Report the malaria status of this cell.
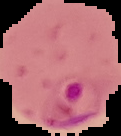
It is parasitized.

image size = 121×136 pixels
preparation = thin blood smear
image type = cell region segmented out of the field of view; surrounding area masked to black